Name the parasite shown.
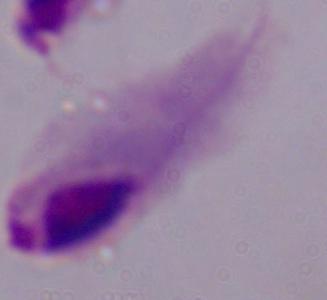
This is a trichomonad.

Summary:
  - Magnification: 1000x
  - Modality: photomicrograph